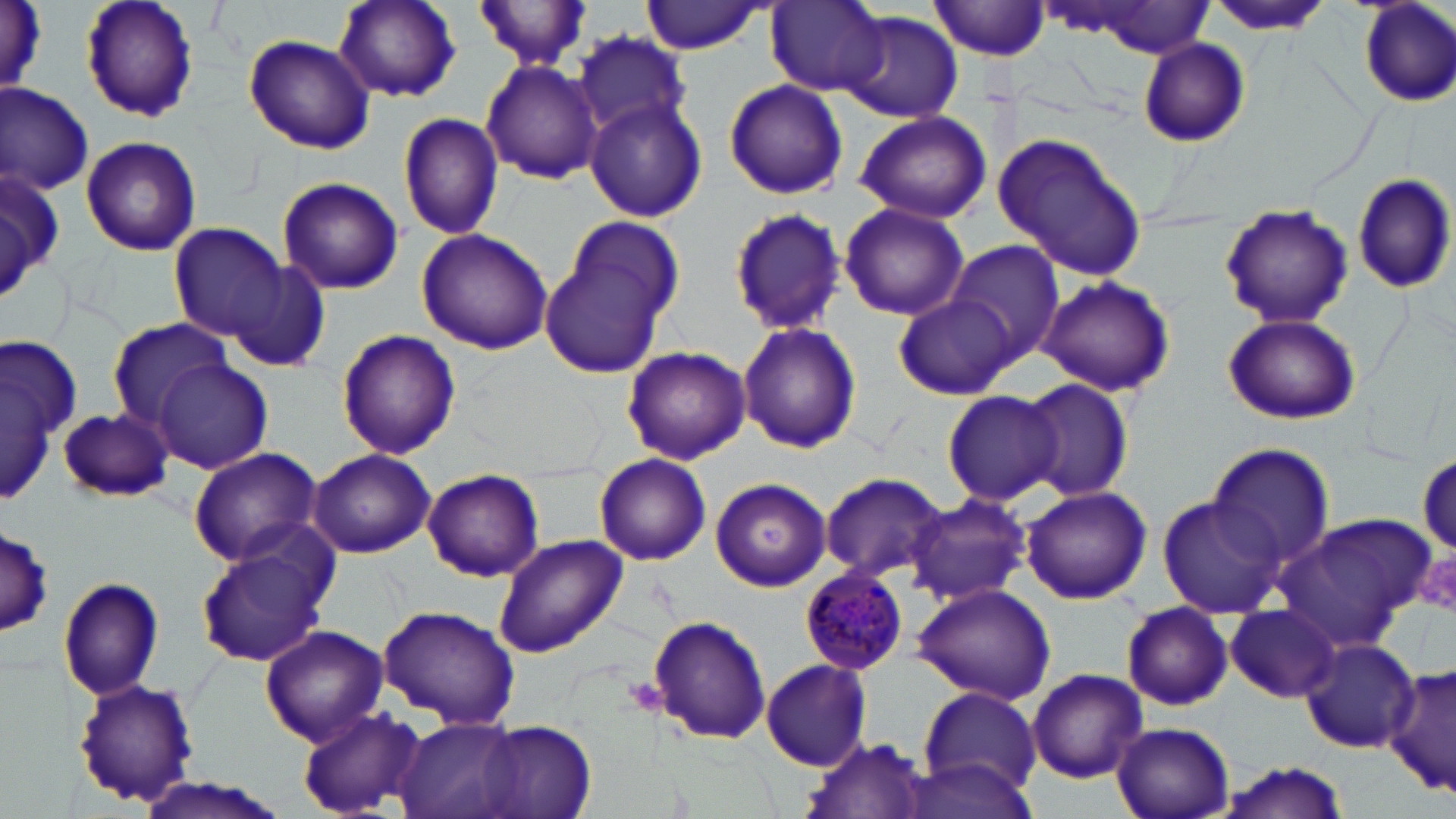

slide-level diagnosis = Plasmodium malariae
stain = May-Grünwald-Giemsa
uninfected red blood cell locations = approximate bounding boxes as (x1,y1)-(x2,y2) corner pairs in pixels: (3,0)-(48,98), (79,0)-(198,124), (333,0)-(462,104), (476,1)-(593,71), (640,1)-(768,54), (765,1)-(888,95), (930,1)-(1052,59), (1354,1)-(1456,109), (1057,3)-(1217,57), (1209,3)-(1329,37), (835,11)-(963,124), (572,32)-(693,142), (242,33)-(375,155), (1137,38)-(1250,149), (480,57)-(602,184), (723,79)-(847,200), (0,83)-(94,193), (585,96)-(708,222), (853,109)-(992,223), (397,111)-(505,241), (991,130)-(1147,283), (79,133)-(202,258), (1,160)-(64,304), (1352,173)-(1454,294), (275,176)-(404,295), (837,200)-(970,322), (1217,205)-(1354,329), (725,207)-(847,334), (543,220)-(682,377), (169,224)-(288,342), (415,228)-(554,355), (944,241)-(1065,363), (223,259)-(333,373), (1038,276)-(1176,397), (892,294)-(1020,401), (1223,315)-(1362,425), (105,319)-(236,427), (736,320)-(862,454), (336,329)-(460,461), (1,341)-(75,505), (620,345)-(750,464), (154,358)-(274,474), (1017,379)-(1135,503), (941,389)-(1063,506), (58,407)-(174,504), (1205,443)-(1336,573), (187,446)-(321,564), (307,449)-(436,559), (594,452)-(711,566), (1414,452)-(1456,554), (420,468)-(545,583), (817,472)-(949,585), (711,478)-(831,592), (1019,486)-(1152,605), (906,495)-(1031,605), (1156,496)-(1283,619), (1272,515)-(1440,650), (1,531)-(55,635), (491,533)-(628,658), (193,534)-(335,668), (58,575)-(165,701), (912,583)-(1056,704), (1120,600)-(1234,712), (375,603)-(521,728), (1226,603)-(1340,702), (647,614)-(771,745), (260,624)-(388,746), (1300,639)-(1422,751), (760,658)-(874,770), (1383,662)-(1455,798), (1026,667)-(1147,783), (72,680)-(200,807), (918,689)-(1041,795), (297,706)-(427,816), (394,714)-(525,819), (1110,719)-(1236,819), (476,721)-(599,819), (801,735)-(933,819), (1217,758)-(1351,819), (903,759)-(1040,818), (132,776)-(292,819)
modality = optical microscopy
magnification = 1000x
Plasmodium malariae-infected red blood cell locations = approximate bounding boxes as (x1,y1)-(x2,y2) corner pairs in pixels: (803,567)-(914,676)
field of view = one of a larger specimen
preparation = thin blood smear
platelet locations = approximate bounding boxes as (x1,y1)-(x2,y2) corner pairs in pixels: (620,677)-(668,717)
image size = 1456×819 pixels